Assess this cell for malaria.
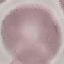
It is uninfected.

image_type: automatically extracted cell patch, resized to 64 × 64 pixels
stain: Giemsa
preparation: thin smear
capture: smartphone through the microscope eyepiece